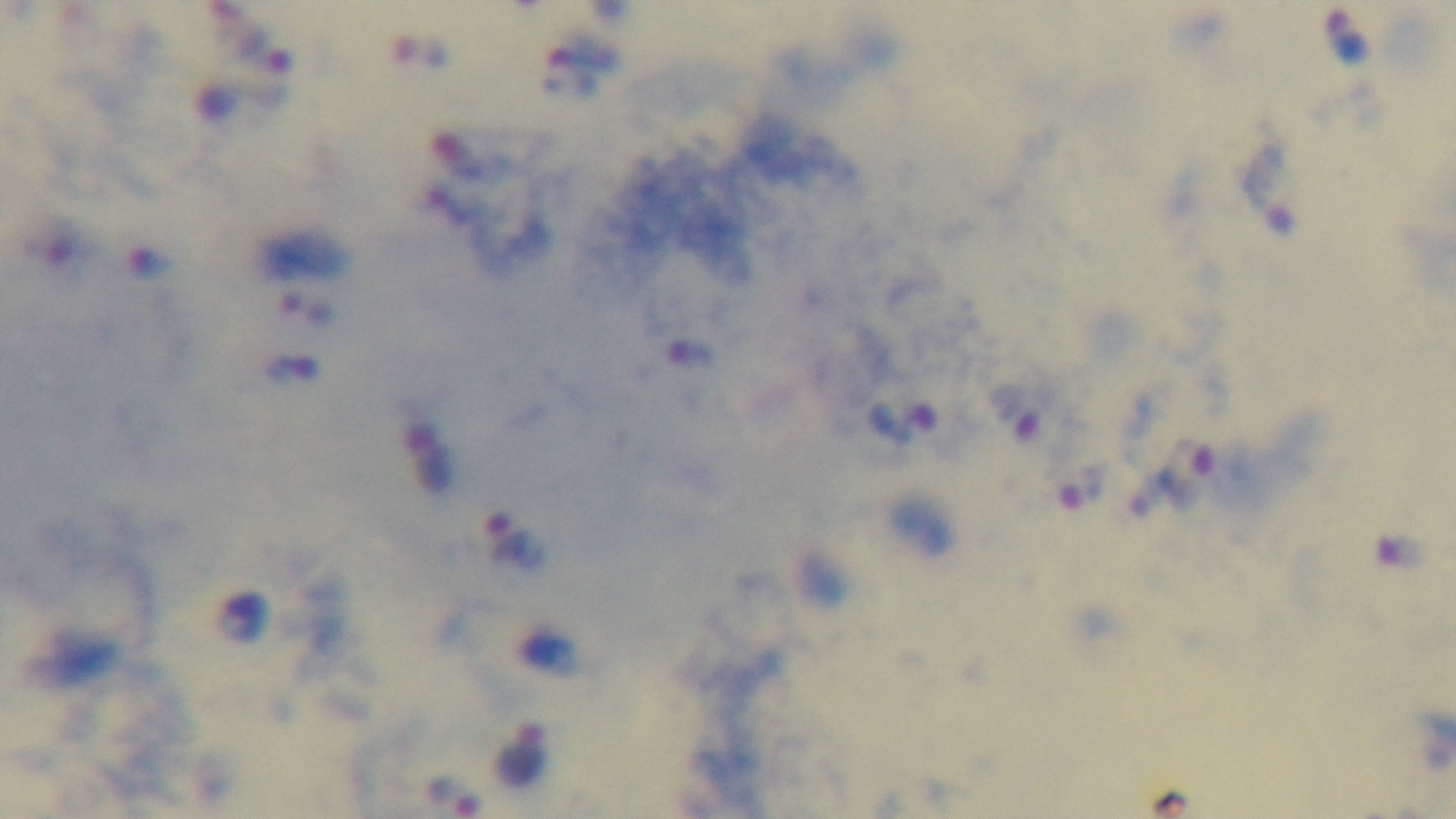
Malaria status: positive. 100x oil-immersion objective. Single field of view. Giemsa stain. Photomicrograph. Captured with a mounted 4K digital camera. Preparation: thick blood film.